Locate every blood parasite and identify its species.
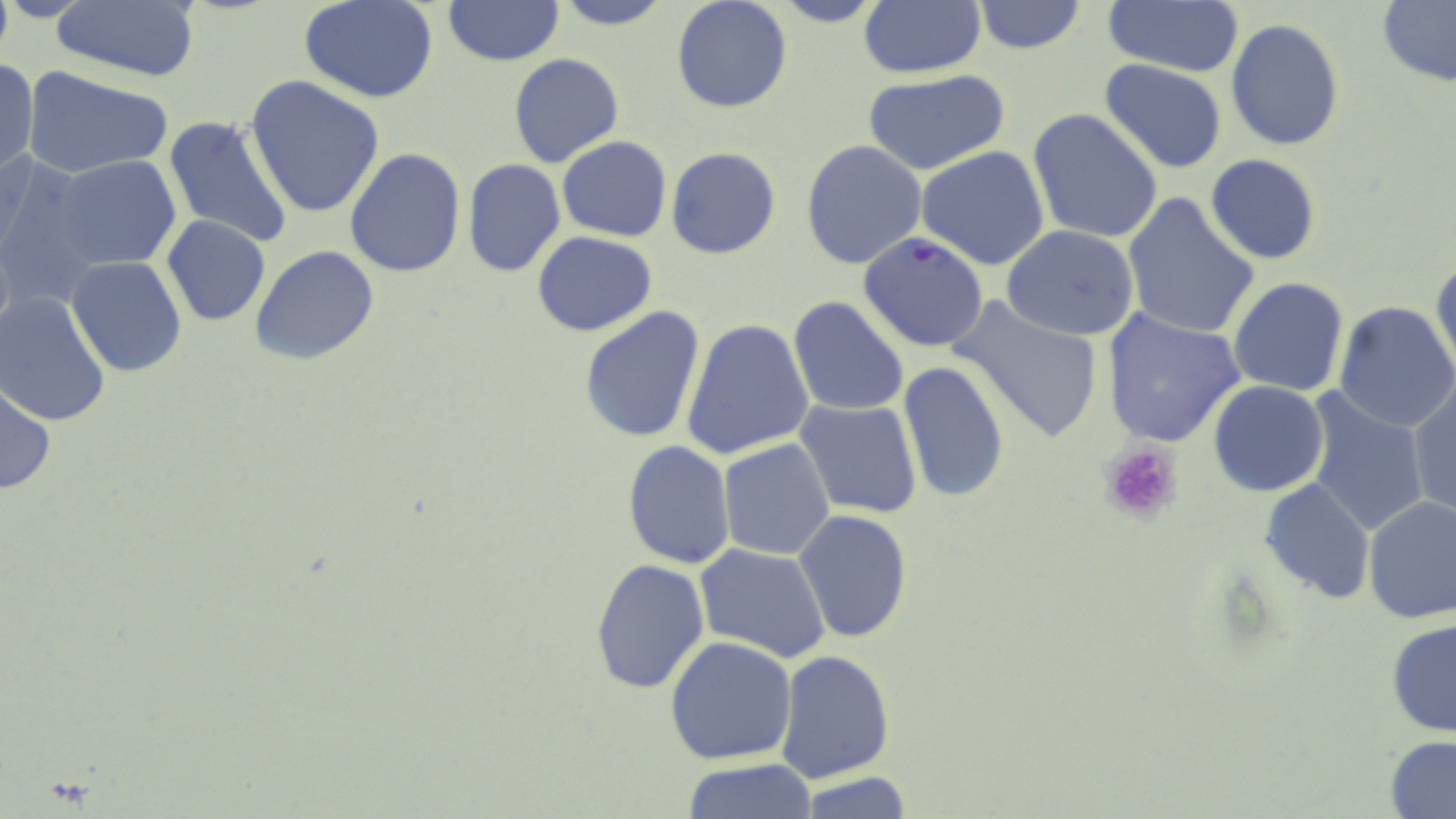

Approximate bounding boxes as named x1/y1/x2/y2 corners in pixels.
Plasmodium falciparum-infected red blood cells: (x1=859, y1=231, x2=988, y2=351).
No Plasmodium ovale, Plasmodium malariae, Plasmodium vivax, Babesia divergens, or Trypanosoma brucei observed.

Summary:
  - Platelet locations: (x1=1098, y1=439, x2=1185, y2=525)
  - Uninfected red blood cell locations: (x1=300, y1=0, x2=440, y2=103), (x1=550, y1=0, x2=678, y2=29), (x1=670, y1=0, x2=793, y2=114), (x1=765, y1=0, x2=892, y2=27), (x1=859, y1=0, x2=986, y2=80), (x1=1378, y1=0, x2=1456, y2=87), (x1=442, y1=1, x2=564, y2=67), (x1=971, y1=1, x2=1087, y2=54), (x1=1102, y1=1, x2=1244, y2=78), (x1=50, y1=2, x2=202, y2=84), (x1=1225, y1=19, x2=1346, y2=152), (x1=492, y1=52, x2=599, y2=248), (x1=508, y1=53, x2=625, y2=170), (x1=1, y1=56, x2=38, y2=178), (x1=1099, y1=58, x2=1229, y2=174), (x1=24, y1=65, x2=175, y2=179), (x1=861, y1=70, x2=1012, y2=177), (x1=246, y1=76, x2=386, y2=219), (x1=1028, y1=108, x2=1164, y2=245), (x1=163, y1=116, x2=295, y2=251), (x1=557, y1=136, x2=671, y2=240), (x1=801, y1=140, x2=926, y2=268), (x1=916, y1=146, x2=1051, y2=270), (x1=665, y1=147, x2=781, y2=260), (x1=345, y1=149, x2=466, y2=279), (x1=1205, y1=152, x2=1322, y2=265), (x1=0, y1=154, x2=104, y2=309), (x1=51, y1=156, x2=180, y2=272), (x1=463, y1=159, x2=566, y2=278), (x1=1120, y1=194, x2=1261, y2=341), (x1=162, y1=216, x2=270, y2=326), (x1=1002, y1=225, x2=1141, y2=342), (x1=532, y1=232, x2=657, y2=336), (x1=251, y1=245, x2=379, y2=367), (x1=1431, y1=254, x2=1455, y2=380), (x1=66, y1=256, x2=187, y2=378), (x1=1227, y1=277, x2=1350, y2=396), (x1=0, y1=293, x2=112, y2=426), (x1=950, y1=296, x2=1105, y2=445), (x1=788, y1=297, x2=910, y2=419), (x1=1332, y1=301, x2=1456, y2=432), (x1=577, y1=305, x2=706, y2=445), (x1=1101, y1=310, x2=1246, y2=448), (x1=680, y1=318, x2=814, y2=461), (x1=897, y1=361, x2=1010, y2=503), (x1=1, y1=379, x2=56, y2=497), (x1=1209, y1=380, x2=1328, y2=497), (x1=1409, y1=381, x2=1455, y2=519), (x1=1301, y1=390, x2=1431, y2=539), (x1=795, y1=398, x2=923, y2=519), (x1=718, y1=439, x2=835, y2=559), (x1=620, y1=441, x2=736, y2=570), (x1=1261, y1=479, x2=1375, y2=605), (x1=1362, y1=496, x2=1456, y2=627), (x1=793, y1=510, x2=913, y2=645), (x1=695, y1=544, x2=833, y2=665), (x1=589, y1=557, x2=710, y2=694), (x1=1386, y1=617, x2=1456, y2=738), (x1=663, y1=634, x2=798, y2=764), (x1=774, y1=649, x2=897, y2=784), (x1=1385, y1=736, x2=1456, y2=817), (x1=682, y1=760, x2=815, y2=817), (x1=793, y1=773, x2=919, y2=817)
  - Slide-level diagnosis: Plasmodium falciparum
  - Stain: May-Grünwald-Giemsa
  - Magnification: 1000x
  - Preparation: thin blood film
  - Field of view: single
  - Modality: light microscopy
  - Image size: 1456×819 pixels